Assess this cell for malaria.
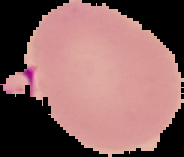
Uninfected.

Summary:
  - Image size: 184×157 pixels
  - Image type: cell region segmented out of the field of view; surrounding area masked to black
  - Preparation: thin blood film